Locate platelets.
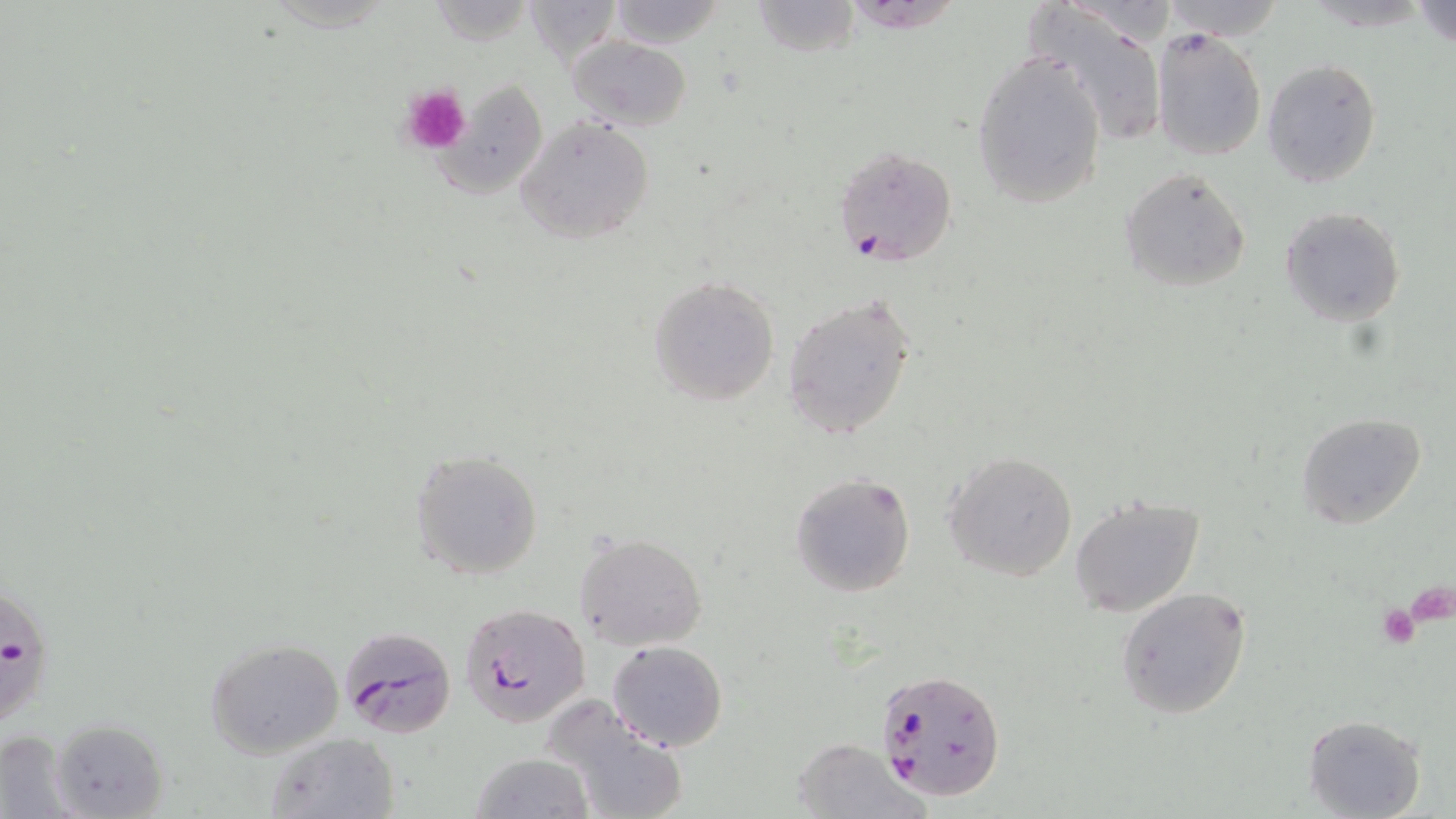

Approximate bounding boxes as (x1,y1)-(x2,y2) corner pairs in pixels.
Platelets: (398,84)-(473,154), (1406,584)-(1456,629), (1376,602)-(1420,649).

Plasmodium falciparum-infected red blood cell locations: (835,145)-(956,266), (0,575)-(57,730), (459,602)-(589,728), (337,624)-(456,738), (873,666)-(1007,801). Uninfected red blood cell locations: (750,0)-(859,56), (1157,0)-(1288,40), (1413,0)-(1456,49), (606,1)-(729,49), (1029,2)-(1168,146), (1153,29)-(1266,161), (568,36)-(691,130), (972,49)-(1109,210), (1262,59)-(1381,187), (435,79)-(548,198), (515,115)-(655,245), (1118,167)-(1251,291), (1279,206)-(1406,327), (648,276)-(780,406), (783,294)-(916,440), (1297,412)-(1425,529), (410,450)-(543,580), (943,451)-(1077,581), (789,471)-(916,598), (1066,495)-(1208,618), (575,532)-(708,650), (1116,587)-(1253,719), (205,638)-(345,756), (608,639)-(727,752), (542,694)-(691,819), (1304,714)-(1427,818), (48,717)-(169,819), (0,730)-(76,815), (266,732)-(398,819), (791,737)-(924,817), (470,753)-(594,819). Slide-level diagnosis: Plasmodium falciparum. 1000x magnification. Single field of view. May-Grünwald-Giemsa stain. Light microscopy. Thin blood film. Image is 1456×819 pixels.